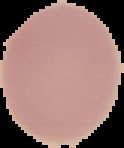
result: no malaria parasites detected
image_type: cell region segmented out of the field of view; surrounding area masked to black
image_size: 124×148 pixels
preparation: thin blood smear